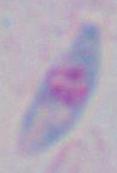
Summary:
  - Identification: Toxoplasma gondii
  - Modality: photomicrograph
  - Magnification: 1000x